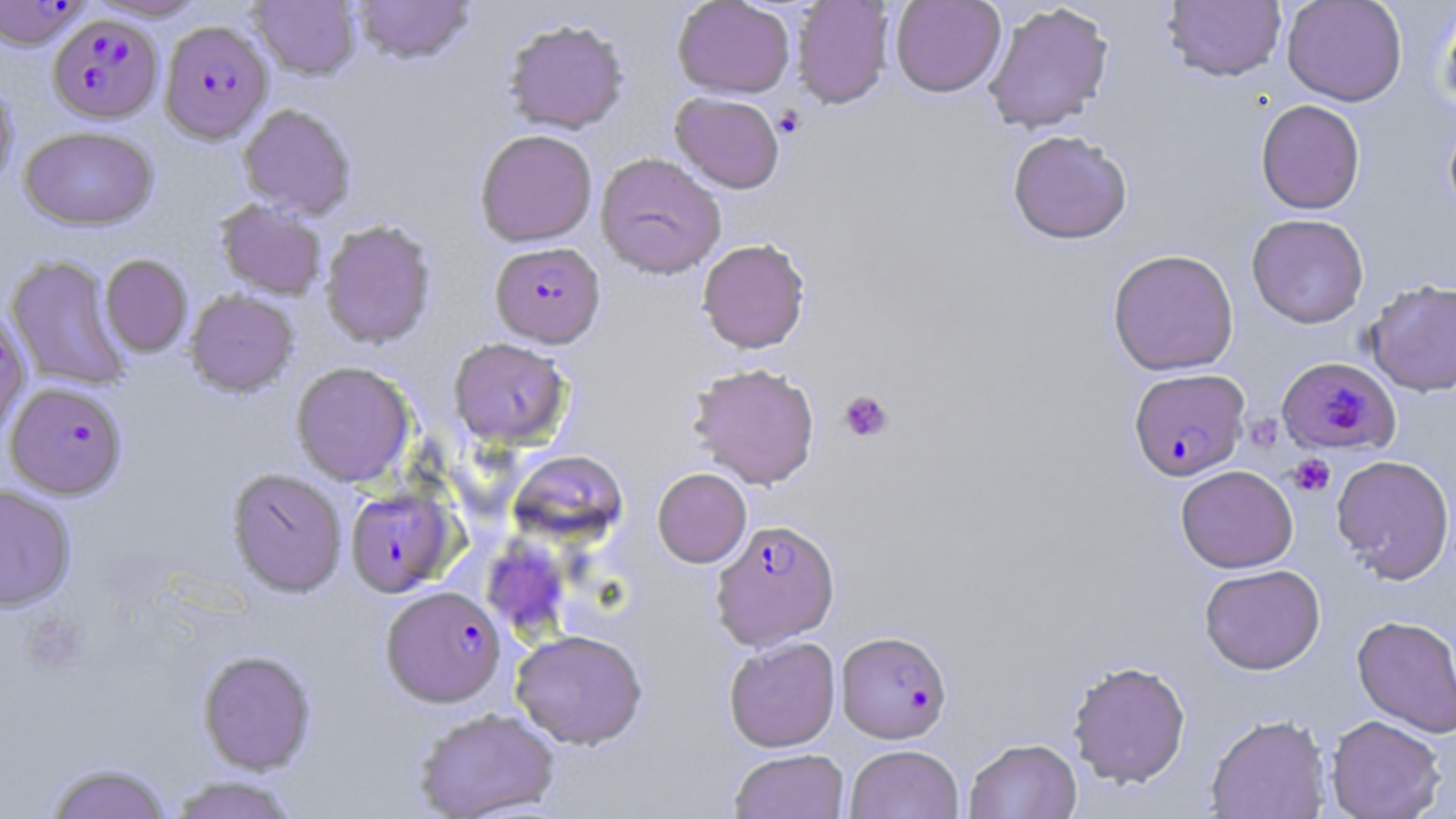

Summary:
  - Coordinate format: approximate bounding boxes as named x1/y1/x2/y2 corners in pixels
  - Plasmodium falciparum-infected red blood cell locations (subset): (x1=0, y1=1, x2=89, y2=51), (x1=48, y1=15, x2=163, y2=124), (x1=159, y1=21, x2=273, y2=144), (x1=490, y1=242, x2=605, y2=348), (x1=1278, y1=356, x2=1401, y2=456), (x1=1130, y1=372, x2=1253, y2=481), (x1=5, y1=382, x2=127, y2=499), (x1=345, y1=487, x2=457, y2=597), (x1=711, y1=518, x2=840, y2=650), (x1=381, y1=585, x2=506, y2=707), (x1=836, y1=630, x2=952, y2=743)
  - Uninfected red blood cell locations (subset): (x1=249, y1=0, x2=361, y2=81), (x1=352, y1=0, x2=475, y2=66), (x1=672, y1=0, x2=795, y2=99), (x1=791, y1=0, x2=895, y2=110), (x1=889, y1=0, x2=1006, y2=97), (x1=1281, y1=0, x2=1407, y2=106), (x1=1162, y1=1, x2=1286, y2=83), (x1=1437, y1=1, x2=1456, y2=117), (x1=982, y1=2, x2=1114, y2=134), (x1=502, y1=18, x2=629, y2=135), (x1=0, y1=79, x2=18, y2=192), (x1=670, y1=92, x2=785, y2=193), (x1=1255, y1=99, x2=1366, y2=214), (x1=238, y1=104, x2=356, y2=219), (x1=1443, y1=107, x2=1456, y2=228), (x1=19, y1=126, x2=159, y2=232), (x1=475, y1=129, x2=598, y2=247), (x1=1007, y1=130, x2=1133, y2=244), (x1=595, y1=152, x2=726, y2=279), (x1=216, y1=201, x2=327, y2=300), (x1=1246, y1=213, x2=1368, y2=328), (x1=320, y1=220, x2=437, y2=349), (x1=697, y1=238, x2=810, y2=353), (x1=1107, y1=248, x2=1239, y2=376), (x1=100, y1=254, x2=192, y2=357), (x1=5, y1=255, x2=131, y2=391), (x1=1364, y1=279, x2=1456, y2=397), (x1=185, y1=290, x2=298, y2=397), (x1=448, y1=338, x2=572, y2=448), (x1=291, y1=361, x2=415, y2=487), (x1=687, y1=362, x2=821, y2=489), (x1=508, y1=450, x2=629, y2=545), (x1=1331, y1=454, x2=1455, y2=583), (x1=1176, y1=465, x2=1298, y2=573), (x1=226, y1=468, x2=348, y2=597), (x1=652, y1=468, x2=751, y2=567), (x1=0, y1=485, x2=76, y2=611), (x1=483, y1=535, x2=570, y2=640), (x1=1199, y1=564, x2=1326, y2=675), (x1=1351, y1=614, x2=1456, y2=738), (x1=510, y1=629, x2=648, y2=749), (x1=723, y1=636, x2=841, y2=752), (x1=197, y1=649, x2=316, y2=774), (x1=1067, y1=659, x2=1191, y2=788), (x1=413, y1=706, x2=560, y2=819), (x1=1205, y1=713, x2=1331, y2=818), (x1=1326, y1=715, x2=1446, y2=819), (x1=964, y1=737, x2=1082, y2=819), (x1=845, y1=744, x2=964, y2=819), (x1=729, y1=748, x2=849, y2=819), (x1=43, y1=761, x2=173, y2=819), (x1=166, y1=774, x2=302, y2=819)
  - Platelet locations: (x1=773, y1=106, x2=805, y2=138), (x1=838, y1=389, x2=894, y2=442), (x1=1252, y1=416, x2=1286, y2=451), (x1=1288, y1=454, x2=1335, y2=497), (x1=23, y1=610, x2=89, y2=673)
  - Slide-level diagnosis: Plasmodium falciparum
  - Preparation: thin blood film
  - Stain: May-Grünwald-Giemsa
  - Image size: 1456×819 pixels
  - Magnification: 1000x
  - Field of view: single
  - Modality: light microscopy